Comment on the morphology of the erythrocytes.
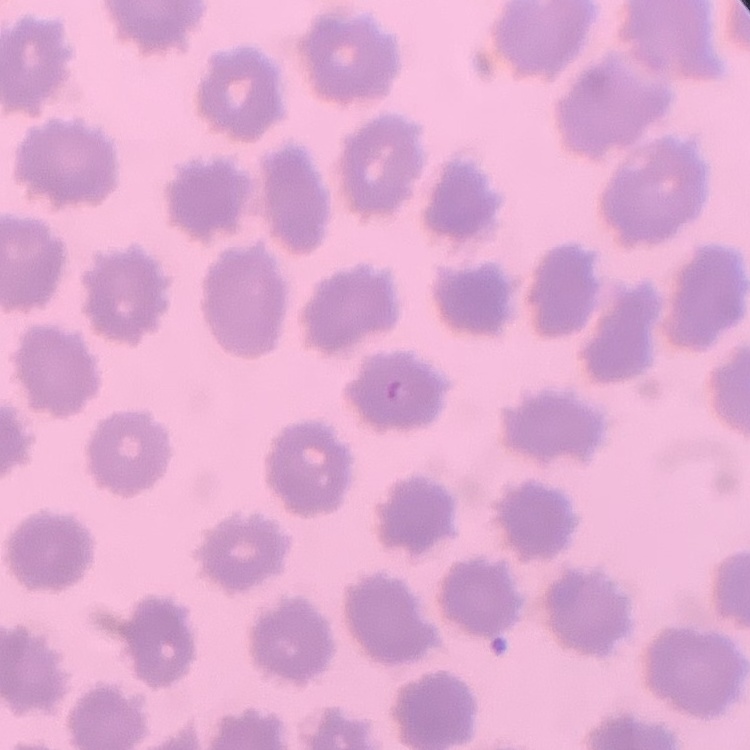

No rouleaux formation.

Summary:
  - Preparation: thin blood film
  - Image type: square crop of a larger photomicrograph
  - Stain: Field's or Giemsa